Identify the parasite.
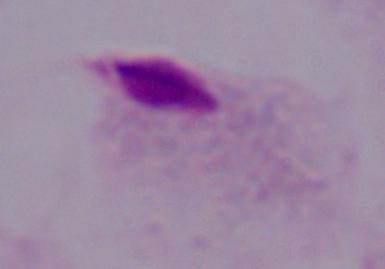

A trichomonad.

Summary:
  - Magnification: 1000x
  - Modality: micrograph